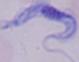
Photomicrograph. A trypanosome is shown. 1000x magnification.